Report the malaria status of this cell.
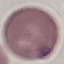
Uninfected.

preparation: thin blood film
image_type: automatically extracted cell patch, resized to 64 × 64 pixels
stain: Giemsa
capture: smartphone camera at the microscope eyepiece